Locate every malaria parasite.
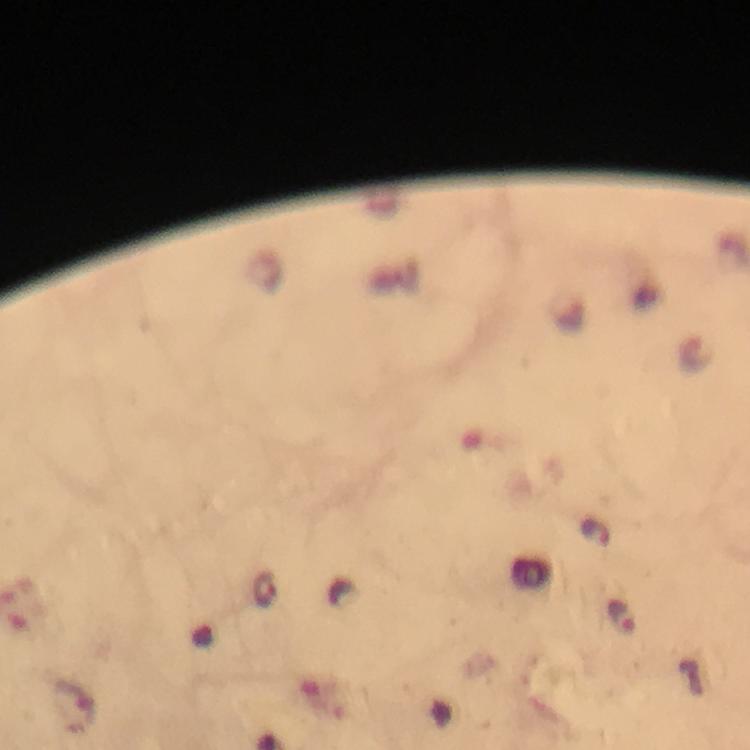

Approximate centers as (x, y) in pixels.
Malaria parasites: (266, 590), (621, 616).

Summary:
  - Context: from a malaria diagnostic workup
  - Capture: smartphone camera through the microscope
  - Image size: 750×750 pixels
  - Stain: Giemsa
  - Magnification: 100x
  - Cropped from: one field of view
  - Preparation: thick smear
  - Immersion oil: applied